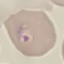

malaria_status: parasitized
image_type: cell patch, automatically extracted from a larger field of view and resized to 64 × 64 pixels
capture: smartphone through the microscope eyepiece
stain: Giemsa
preparation: thin smear